Locate every malaria parasite.
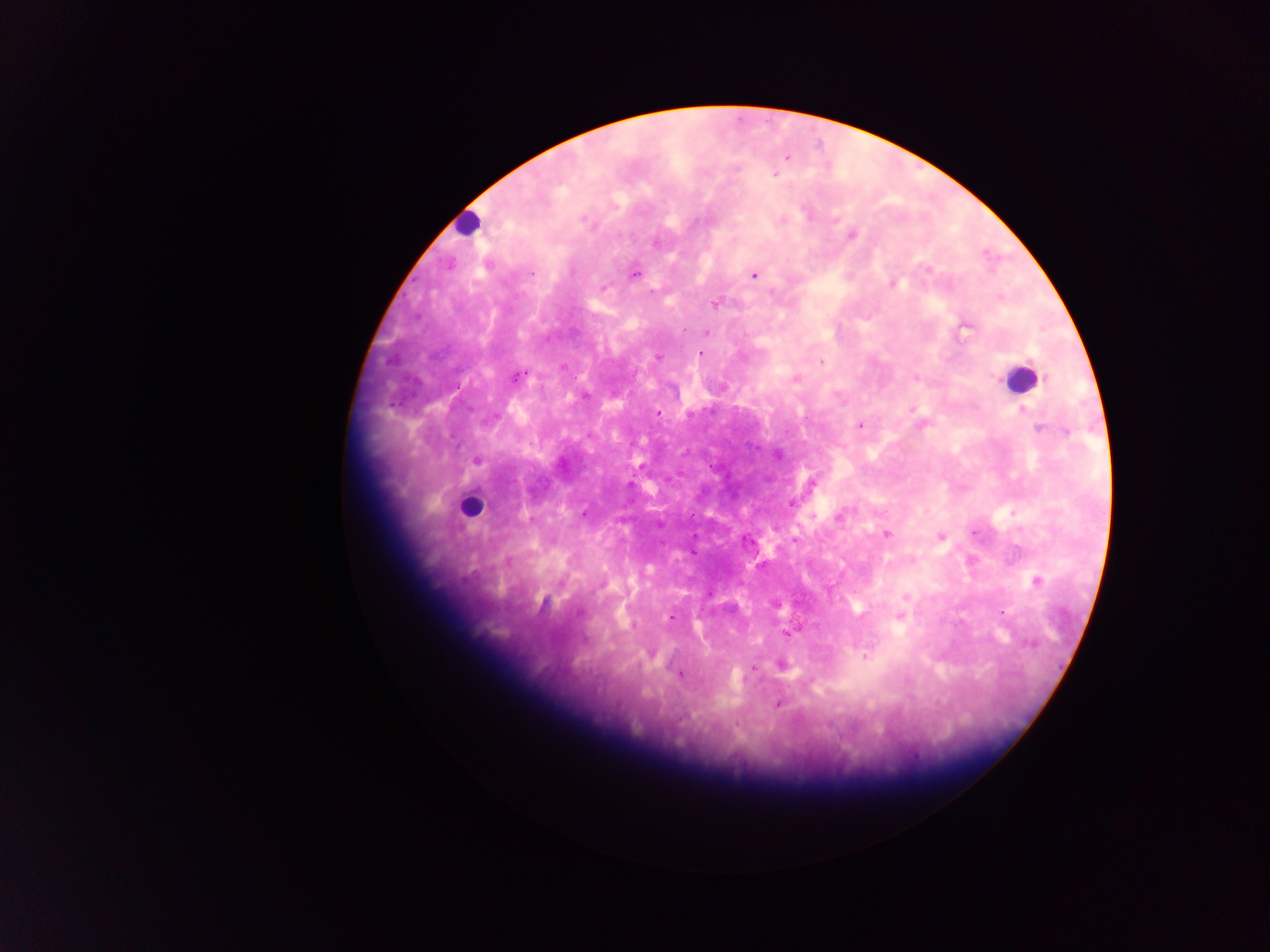
Approximate centers as (x, y) in pixels.
Malaria parasites: (787, 157), (775, 174), (615, 207), (805, 212), (584, 220), (783, 220), (834, 220), (853, 236), (656, 243), (927, 269), (572, 271), (532, 274), (634, 275), (753, 275), (892, 285), (604, 287), (715, 304), (964, 327), (707, 332), (701, 354), (658, 357), (821, 362), (563, 366), (519, 376), (916, 378), (796, 379), (912, 409), (1023, 411), (658, 413), (860, 426), (1038, 429), (452, 437), (476, 461), (813, 484), (791, 504), (583, 513), (839, 517), (974, 533), (886, 534), (940, 536), (795, 540), (1036, 581), (906, 597), (1004, 611), (670, 617), (900, 617), (788, 634), (865, 657), (753, 667), (681, 674), (778, 705), (736, 723).

{
  "image_size": "1270×952 pixels",
  "capture": "mobile-phone photograph through a microscope",
  "country": "Ghana",
  "preparation": "thick blood film",
  "field_of_view": "single",
  "leukocyte_locations": "approximate centers as (x, y) in pixels: (466, 223), (1020, 379), (469, 507)"
}